Point out cells.
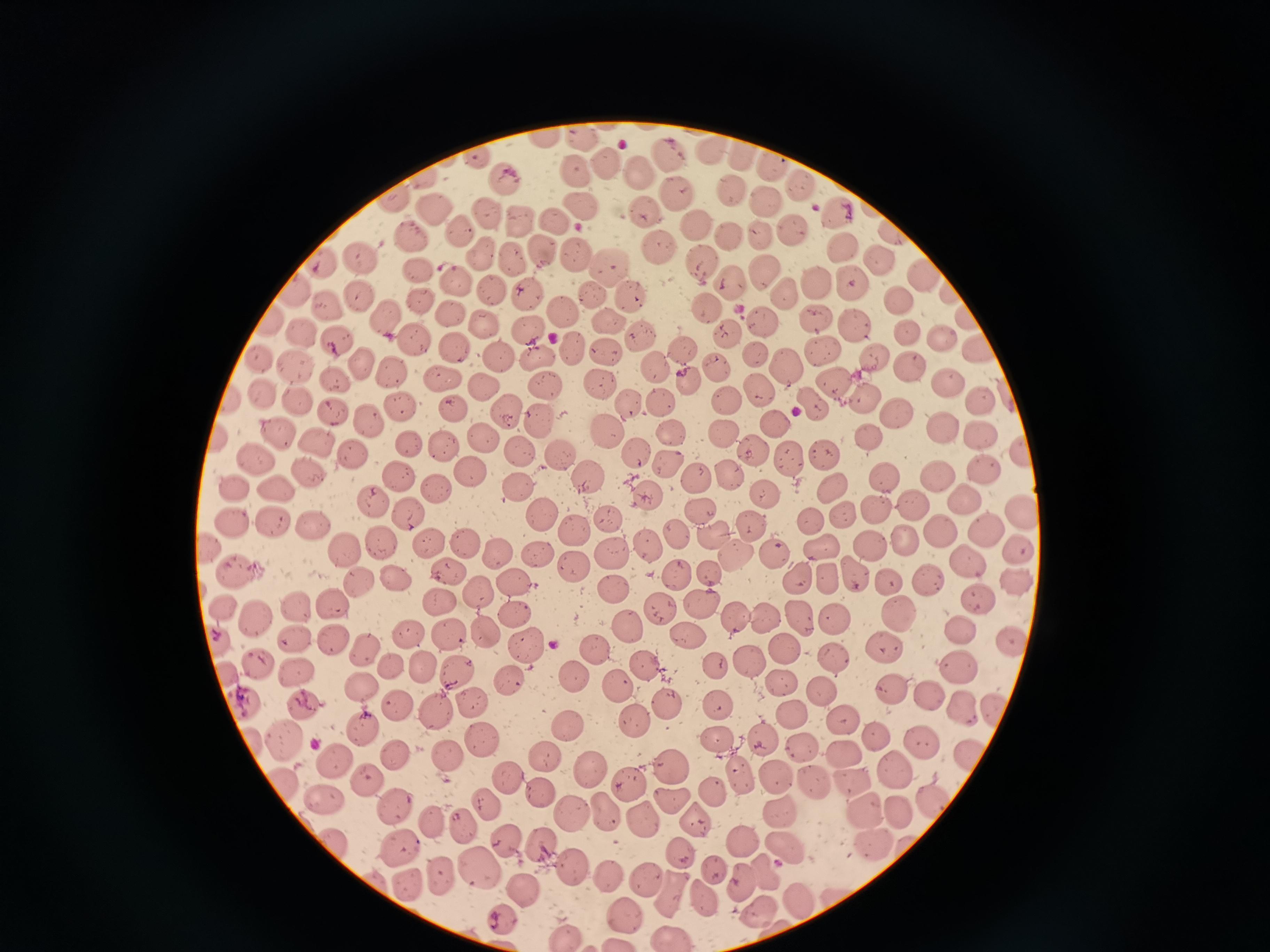
Approximate centers as [x, y] in pixels.
Cells: [546, 135], [579, 140], [711, 146], [665, 154], [478, 157], [741, 157], [604, 161], [771, 166], [638, 169], [573, 172], [423, 179], [510, 183], [798, 185], [730, 186], [676, 190], [389, 198], [766, 199], [580, 206], [835, 207], [643, 208], [488, 211], [435, 212], [558, 216], [521, 221], [694, 223], [796, 229], [464, 231], [763, 232], [729, 233], [893, 233], [413, 238], [842, 241], [657, 242], [538, 251], [577, 254], [483, 256], [883, 257], [359, 258], [512, 260], [702, 260], [322, 263], [611, 266], [765, 268], [420, 273], [922, 275], [455, 278], [729, 282], [817, 282], [854, 284], [948, 289], [293, 290], [492, 292], [530, 293], [357, 294], [787, 294], [594, 295], [632, 297], [900, 299], [422, 302], [330, 305], [709, 308], [454, 309], [564, 310], [385, 313], [966, 314], [609, 315], [816, 317], [764, 318], [857, 319], [269, 323], [486, 323], [528, 326], [639, 330], [302, 333], [907, 333], [732, 334], [939, 337], [417, 339], [457, 343], [980, 344], [577, 345], [338, 346], [680, 347], [819, 347], [609, 351], [538, 352], [261, 355], [498, 355], [753, 355], [871, 356], [715, 358], [357, 362], [294, 363], [785, 363], [392, 367], [655, 369], [912, 369], [443, 375], [688, 376], [598, 379], [833, 380], [945, 380], [335, 381], [483, 383], [547, 383], [759, 389], [298, 393], [264, 394], [728, 395], [866, 397], [979, 398], [660, 403], [815, 403], [628, 405], [453, 406], [398, 407], [510, 407], [332, 411], [897, 412], [539, 415], [368, 418], [776, 425], [938, 426], [605, 427], [980, 429], [282, 430], [667, 430], [723, 432], [870, 434], [482, 439], [318, 440], [408, 443], [444, 444], [522, 449], [558, 449], [753, 449], [355, 450], [1023, 450], [637, 451], [823, 454], [791, 459], [666, 463], [256, 464], [980, 464], [470, 470], [881, 472], [308, 473], [733, 474], [936, 474], [584, 475], [697, 476], [403, 479], [431, 484], [832, 484], [512, 486], [273, 488], [236, 490], [644, 492], [763, 492], [962, 497], [373, 501], [913, 502], [872, 506], [698, 509], [541, 513], [842, 513], [1022, 516], [408, 517], [810, 518], [609, 519], [268, 521], [755, 524], [233, 525], [574, 526], [312, 528], [982, 529], [942, 530], [712, 532], [675, 534], [377, 539], [430, 541], [464, 542], [905, 542], [206, 545], [646, 545], [819, 546], [872, 546], [1018, 547], [345, 548], [537, 548], [614, 552], [735, 553], [497, 554], [774, 558], [967, 560], [575, 566], [448, 570], [236, 571], [854, 571], [675, 573], [799, 574], [710, 575], [823, 577], [392, 578], [517, 579], [889, 579], [930, 579], [1015, 579], [364, 587], [611, 588], [477, 592], [975, 598], [438, 601], [335, 603], [664, 603], [700, 604], [221, 606], [297, 607], [899, 612], [258, 613], [514, 613], [736, 614], [798, 615], [831, 616], [770, 618], [627, 626], [484, 627], [963, 627], [448, 631], [407, 632], [693, 638], [1010, 638], [299, 641], [217, 642], [334, 644], [528, 644], [364, 647], [882, 648], [596, 649], [780, 649], [832, 652], [261, 659], [745, 659], [644, 661], [716, 662], [390, 664], [425, 666], [458, 667], [960, 667], [229, 671], [295, 673], [577, 674], [510, 680], [778, 683], [893, 684], [365, 685], [620, 686], [824, 688], [932, 694], [470, 700], [247, 701], [399, 703], [307, 705], [717, 705], [668, 706], [962, 706], [996, 706], [436, 709], [794, 712], [840, 719], [635, 720], [566, 722], [364, 730], [874, 734], [765, 735], [487, 738], [921, 738], [718, 739], [285, 740], [801, 751], [843, 751], [392, 753], [450, 754], [549, 754], [971, 754], [336, 761], [670, 762], [587, 763], [894, 765], [773, 772], [505, 777], [740, 777], [850, 779], [812, 780], [368, 781], [627, 782], [540, 791], [713, 792], [326, 798], [674, 798], [932, 800], [395, 802], [487, 803], [901, 807], [611, 809], [572, 810], [863, 810], [784, 811], [432, 817], [646, 817], [460, 821], [698, 821], [507, 838], [338, 840], [741, 840], [539, 841], [874, 845], [788, 846], [398, 848], [683, 849], [479, 864], [572, 864], [717, 870], [765, 872], [440, 874], [646, 875], [606, 878], [742, 880], [408, 882], [524, 888], [675, 891], [707, 896], [798, 898], [758, 908], [622, 912], [564, 931], [672, 933].

One field from this slide. Photographed with a smartphone camera at the microscope eyepiece. Giemsa-stained preparation. Thin blood film. Image is 1270×952 pixels.